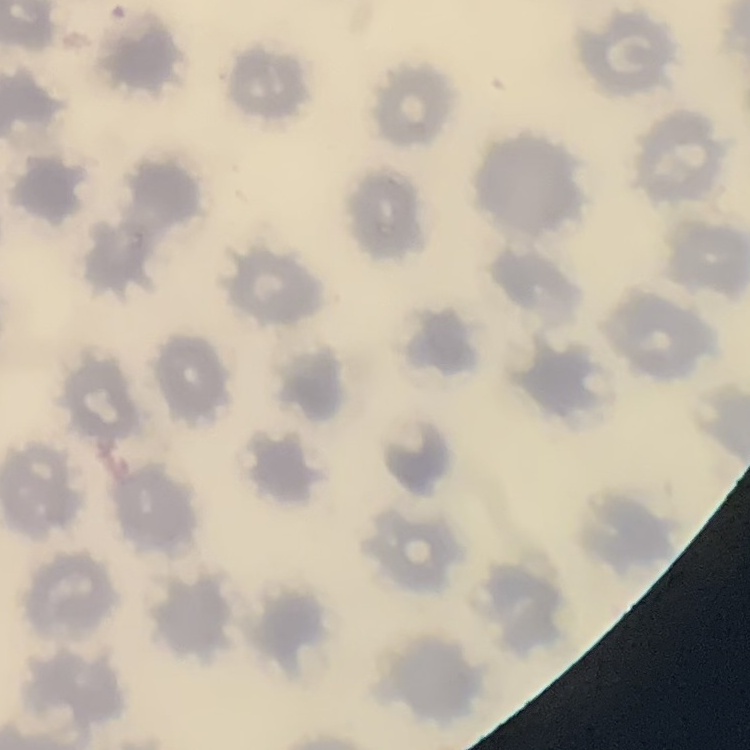

red blood cell morphology = no rouleaux formation
preparation = thin blood film
image type = square crop of a larger photomicrograph
stain = Field's or Giemsa